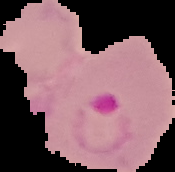

Malaria status: parasitized. Image is 175×172 pixels. Segmented cell region on a black background. From a thin blood film.